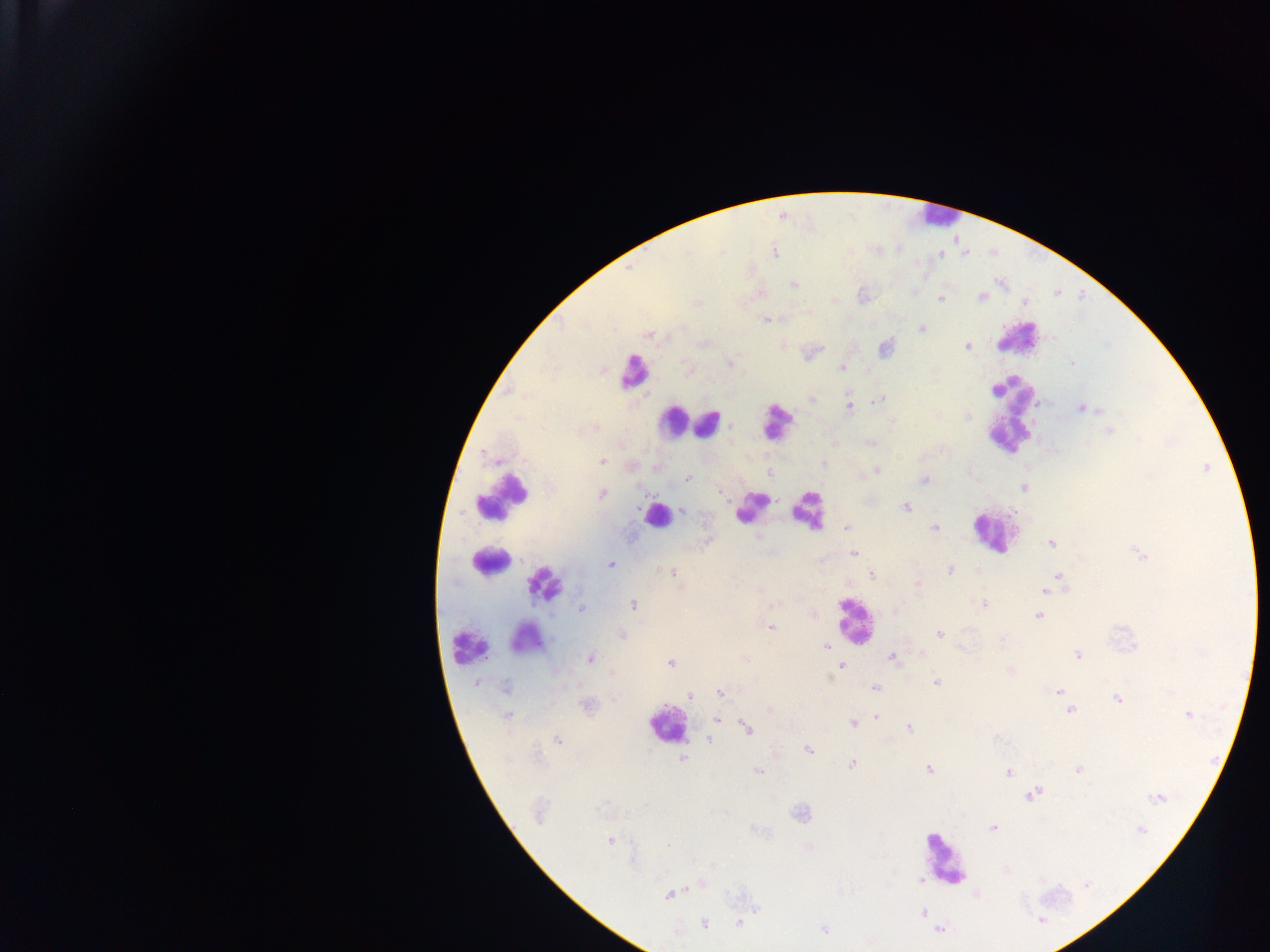

Approximate centers as {x, y} in pixels.
Summary:
  - Leukocyte locations: {934, 215}, {1017, 343}, {632, 373}, {1009, 416}, {672, 422}, {774, 422}, {711, 424}, {502, 497}, {751, 508}, {810, 513}, {655, 515}, {989, 537}, {491, 560}, {546, 579}, {848, 621}, {537, 636}, {472, 643}, {947, 859}
  - Malaria parasite locations: {774, 252}, {793, 285}, {981, 297}, {939, 298}, {1025, 304}, {766, 320}, {922, 328}, {648, 334}, {967, 345}, {730, 361}, {843, 368}, {996, 390}, {810, 398}, {879, 400}, {849, 408}, {1102, 409}, {1083, 410}, {968, 416}, {893, 420}, {594, 429}, {1110, 430}, {485, 455}, {489, 460}, {602, 463}, {876, 470}, {687, 479}, {925, 480}, {601, 495}, {906, 507}, {683, 510}, {845, 528}, {934, 528}, {1052, 544}, {853, 552}, {611, 565}, {949, 569}, {672, 573}, {871, 574}, {1059, 575}, {1045, 591}, {633, 605}, {984, 605}, {582, 609}, {1039, 614}, {770, 628}, {623, 634}, {940, 634}, {1003, 640}, {826, 645}, {1077, 655}, {894, 657}, {591, 659}, {670, 662}, {842, 666}, {937, 682}, {479, 685}, {877, 688}, {505, 689}, {1058, 692}, {719, 693}, {689, 696}, {1116, 700}, {1067, 704}, {1070, 709}, {1186, 715}, {877, 716}, {507, 717}, {718, 719}, {852, 724}, {747, 726}, {909, 727}, {557, 738}, {711, 741}, {808, 750}, {682, 759}, {852, 764}, {1077, 770}, {929, 771}, {759, 772}, {1008, 772}, {1032, 794}, {1158, 800}, {993, 829}, {1140, 830}, {610, 840}, {669, 846}, {921, 878}, {670, 894}, {924, 912}, {1042, 919}, {739, 923}, {703, 924}, {824, 928}, {940, 928}
  - Object labeled both malaria parasite and leukocyte by the source: {664, 723}
  - Preparation: thick blood film
  - Capture: mobile-phone photograph through a microscope
  - Field of view: single
  - Image size: 1270×952 pixels
  - Country: Ghana